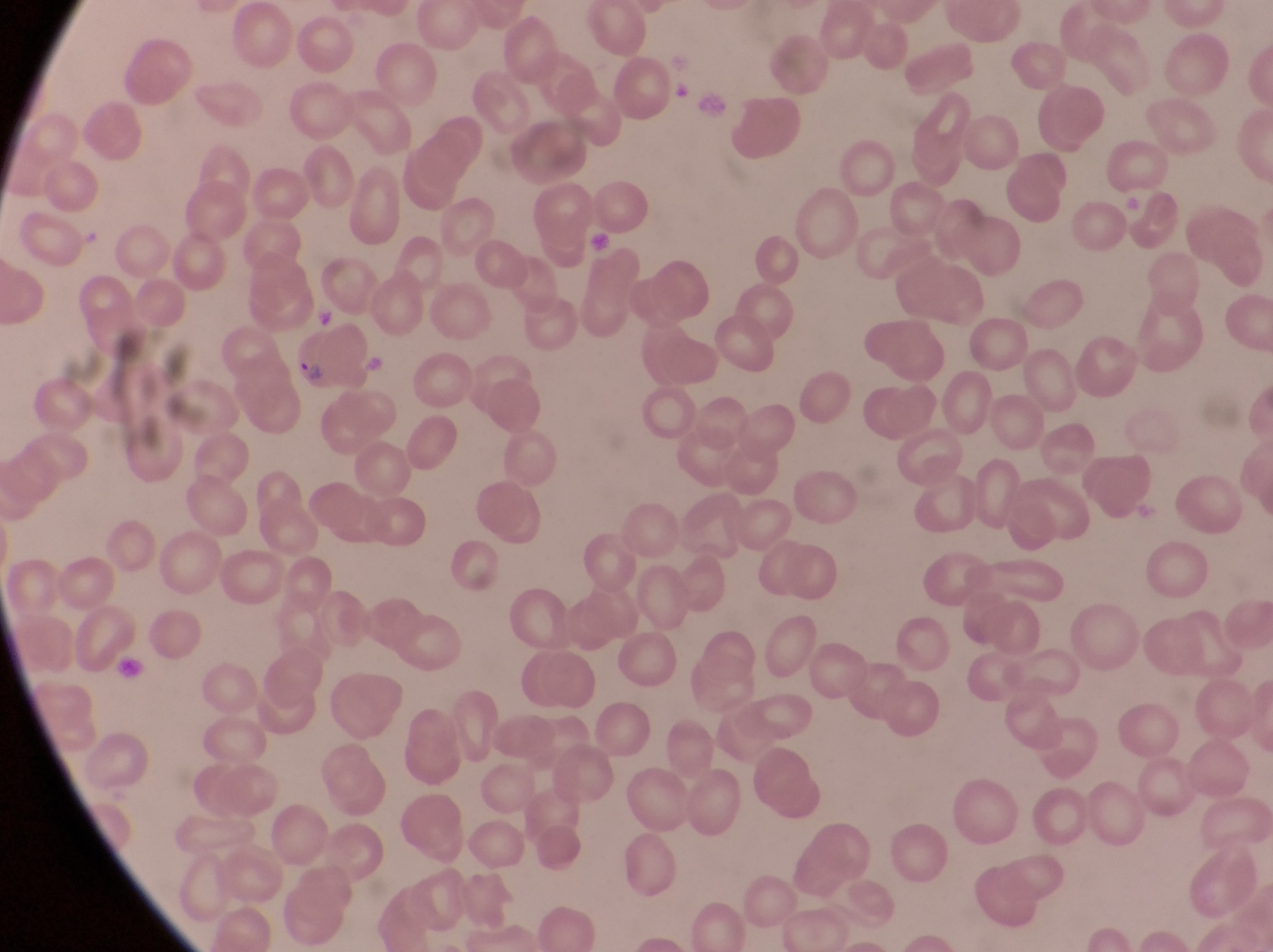
Approximate bounding boxes as [left, top, right, bottom] in pixels. Parasitised red blood cell locations: [285, 317, 373, 394]. Artifact (platelet-like body, stain precipitate, or debris) locations: [587, 223, 619, 255], [116, 657, 147, 681]. Thin blood film. Image is 1273×952 pixels. Photographed through the eyepiece of an Olympus CX-23 microscope with a smartphone camera. One field of view. Magnification of 1000x. Collected in Uganda.